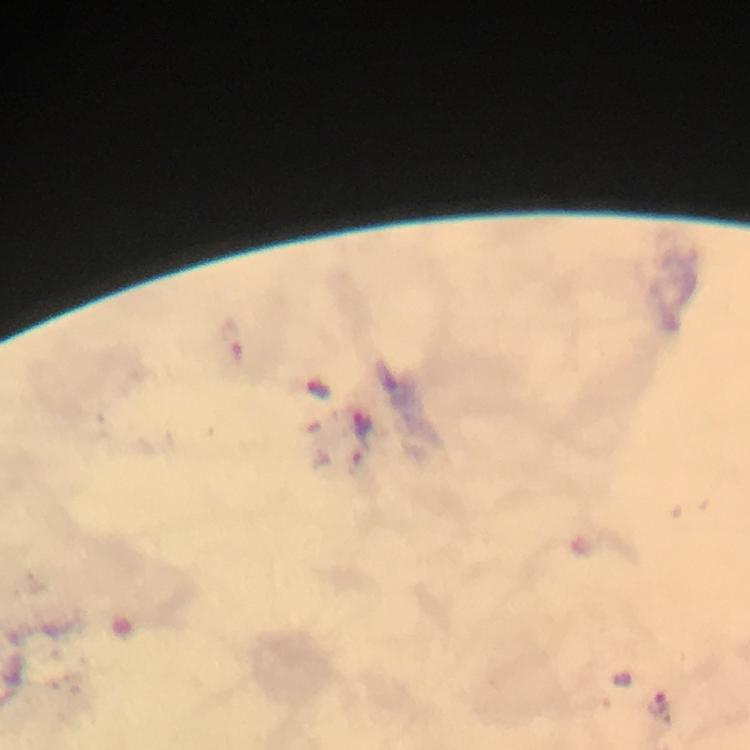

Approximate centers as [x, y] in pixels. Plasmodium parasite locations: [362, 426], [658, 704]. Photographed through the microscope with a smartphone camera. Giemsa stain. Immersion oil was used. From a malaria diagnostic workup. At 100x magnification. A crop from one field of view. Image is 750×750 pixels. Thick blood smear.